Classify this cell by malaria status.
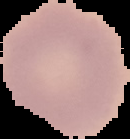
Uninfected.

preparation = thin blood film
image size = 130×139 pixels
image type = segmented cell region on a black background